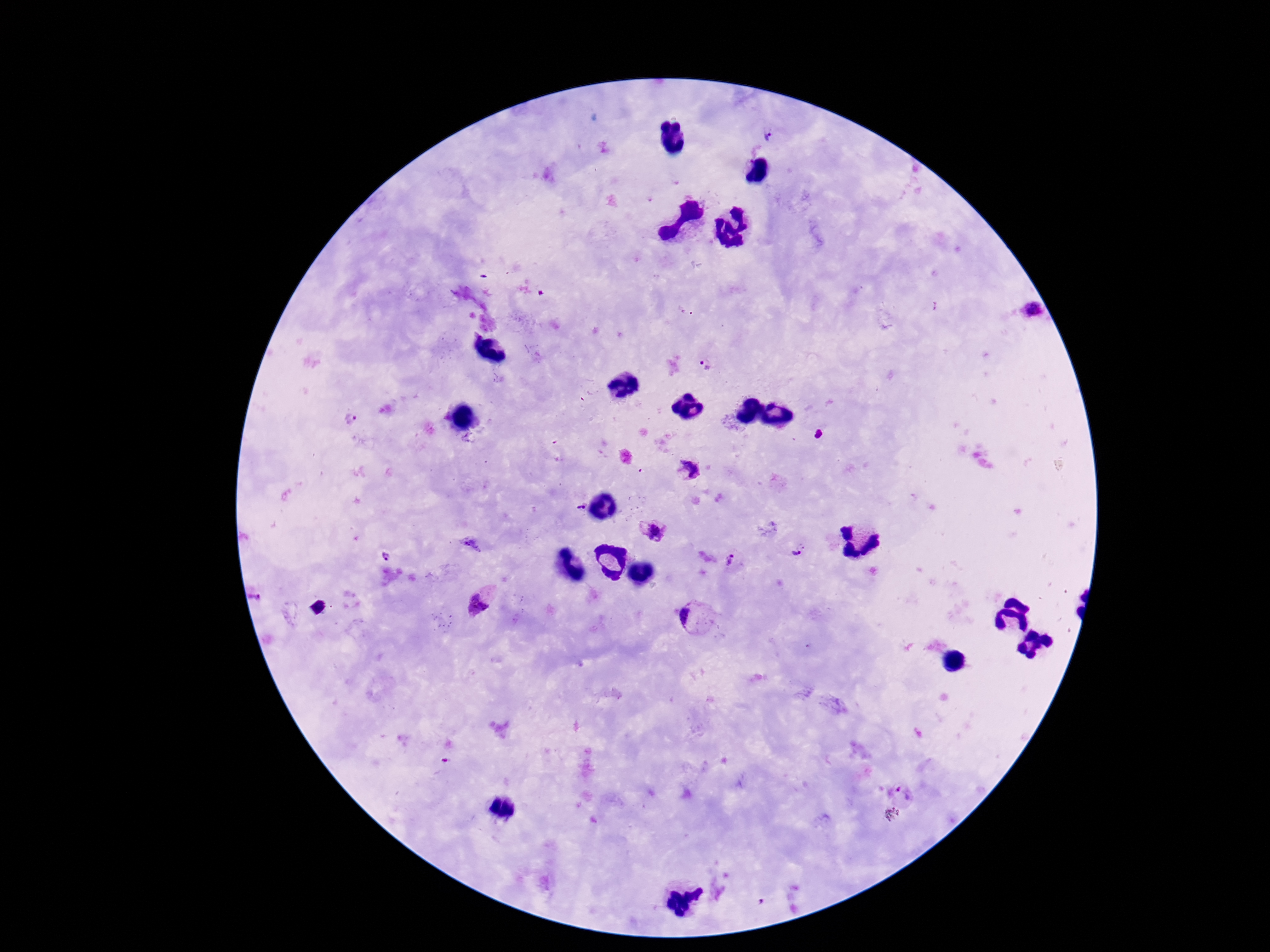

Approximate centers as {x, y} in pixels. Plasmodium parasite locations: {766, 137}, {1029, 309}, {706, 364}, {351, 420}, {688, 470}, {580, 507}, {654, 533}, {469, 544}, {797, 552}, {387, 558}, {730, 560}, {477, 605}, {690, 616}, {902, 794}. Thick blood smear. Single field of view. Patient malaria status: positive. Smartphone photograph taken through the microscope eyepiece. Image is 1270×952 pixels. 100x magnification. Giemsa stain.